Classify this cell by malaria status.
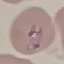
Parasitized.

stain = Giemsa
capture = smartphone camera at the microscope eyepiece
preparation = thin blood film
image type = automatically extracted cell patch, resized to 64 × 64 pixels